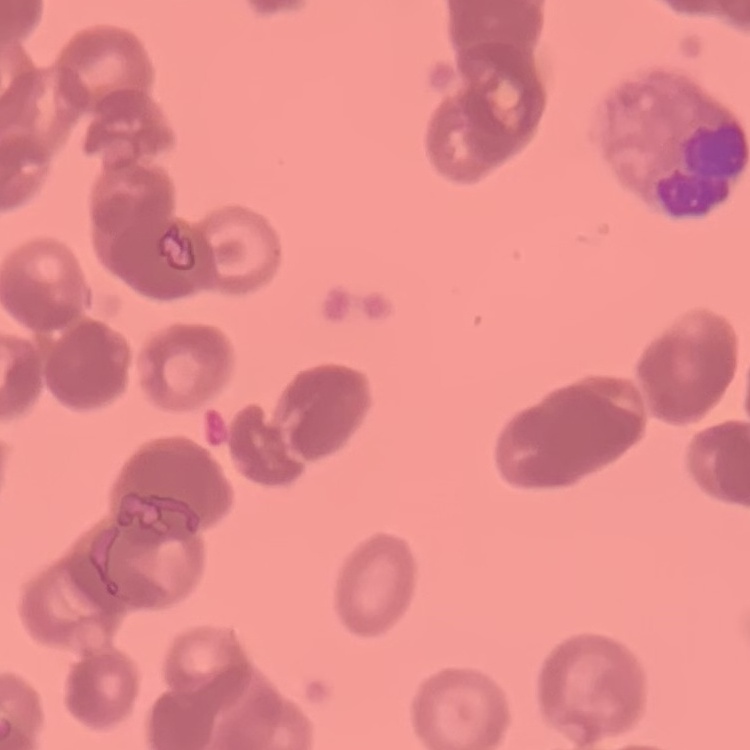
erythrocyte morphology = rouleaux formation
preparation = thin blood smear
stain = Field's or Giemsa
image type = one tile cut from a larger photomicrograph